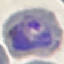

Summary:
  - Malaria status: parasitized
  - Preparation: thin smear
  - Image type: automatically extracted cell patch, resized to 64 × 64 pixels
  - Capture: smartphone through the microscope eyepiece
  - Stain: Giemsa